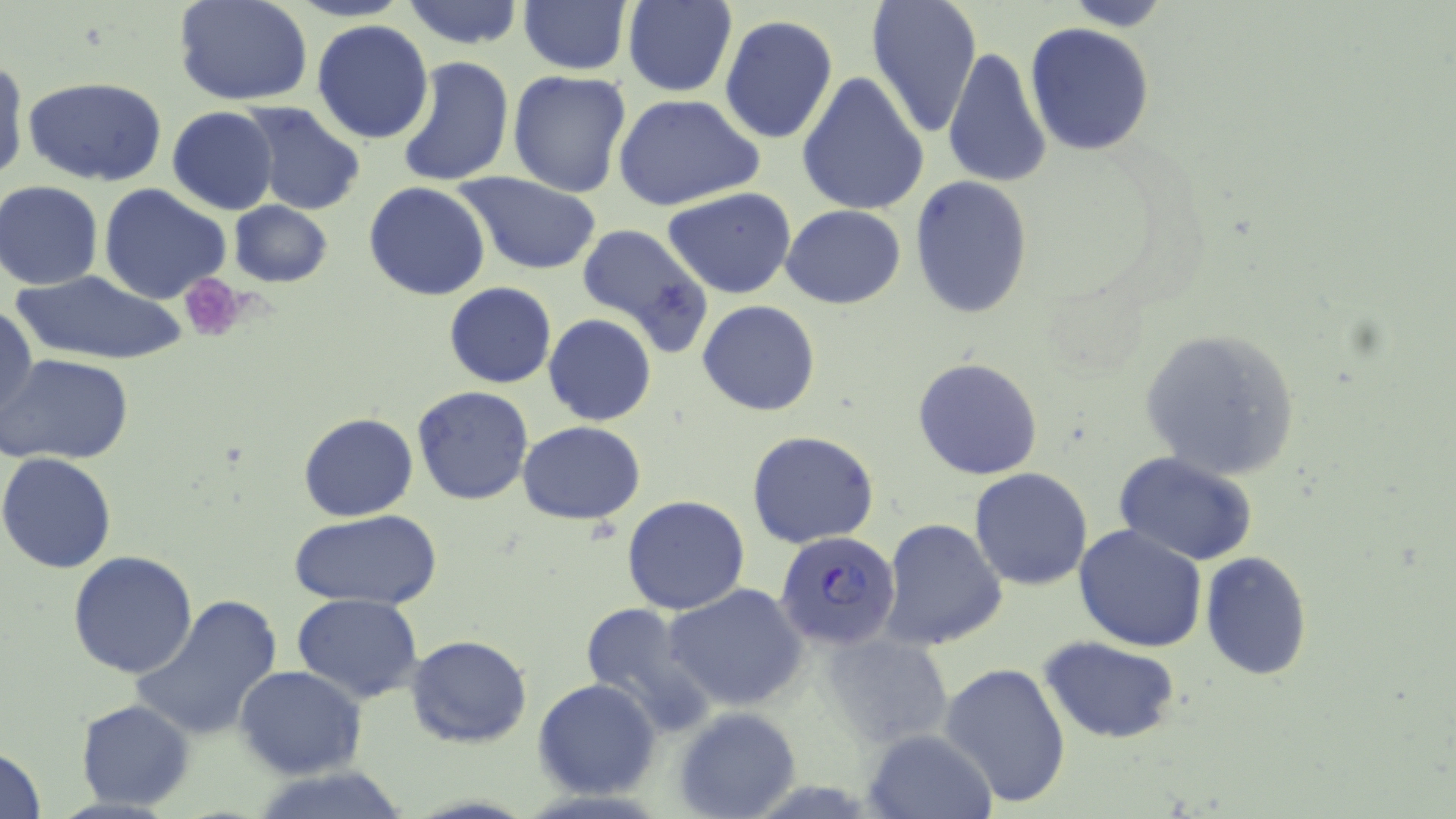
slide-level diagnosis = Plasmodium falciparum
image size = 1456×819 pixels
preparation = thin blood smear
modality = light microscopy
magnification = 1000x
uninfected red blood cell locations = approximate bounding boxes as named x1/y1/x2/y2 corners in pixels: (x1=173, y1=0, x2=314, y2=105), (x1=287, y1=0, x2=413, y2=22), (x1=401, y1=0, x2=525, y2=51), (x1=865, y1=0, x2=984, y2=138), (x1=1056, y1=0, x2=1177, y2=29), (x1=622, y1=2, x2=736, y2=97), (x1=519, y1=3, x2=631, y2=75), (x1=719, y1=16, x2=839, y2=144), (x1=312, y1=19, x2=435, y2=144), (x1=1025, y1=23, x2=1155, y2=157), (x1=942, y1=46, x2=1051, y2=189), (x1=0, y1=56, x2=26, y2=186), (x1=397, y1=56, x2=514, y2=188), (x1=507, y1=71, x2=632, y2=197), (x1=797, y1=71, x2=931, y2=216), (x1=24, y1=77, x2=168, y2=186), (x1=613, y1=92, x2=764, y2=212), (x1=239, y1=101, x2=366, y2=215), (x1=167, y1=106, x2=278, y2=215), (x1=456, y1=171, x2=605, y2=274), (x1=910, y1=177, x2=1034, y2=319), (x1=1, y1=181, x2=104, y2=289), (x1=364, y1=182, x2=490, y2=301), (x1=99, y1=183, x2=231, y2=304), (x1=662, y1=187, x2=797, y2=299), (x1=229, y1=201, x2=333, y2=289), (x1=781, y1=203, x2=907, y2=308), (x1=574, y1=221, x2=714, y2=358), (x1=9, y1=271, x2=187, y2=367), (x1=444, y1=282, x2=556, y2=388), (x1=432, y1=285, x2=543, y2=493), (x1=698, y1=300, x2=821, y2=417), (x1=1, y1=304, x2=37, y2=428), (x1=542, y1=314, x2=656, y2=426), (x1=1138, y1=327, x2=1301, y2=481), (x1=1, y1=354, x2=133, y2=465), (x1=912, y1=357, x2=1044, y2=481), (x1=411, y1=385, x2=535, y2=505), (x1=299, y1=413, x2=418, y2=522), (x1=517, y1=421, x2=645, y2=524), (x1=747, y1=430, x2=879, y2=549), (x1=0, y1=452, x2=119, y2=573), (x1=1115, y1=453, x2=1258, y2=567), (x1=968, y1=468, x2=1092, y2=590), (x1=1092, y1=477, x2=1253, y2=632), (x1=621, y1=495, x2=750, y2=615), (x1=291, y1=508, x2=443, y2=609), (x1=879, y1=519, x2=1006, y2=652), (x1=1074, y1=523, x2=1207, y2=652), (x1=67, y1=551, x2=198, y2=678), (x1=1201, y1=552, x2=1313, y2=679), (x1=663, y1=583, x2=809, y2=713), (x1=291, y1=594, x2=423, y2=705), (x1=130, y1=595, x2=286, y2=742), (x1=576, y1=602, x2=714, y2=735), (x1=824, y1=627, x2=953, y2=748), (x1=406, y1=636, x2=531, y2=748), (x1=1041, y1=637, x2=1181, y2=744), (x1=940, y1=660, x2=1072, y2=809), (x1=235, y1=666, x2=366, y2=779), (x1=534, y1=678, x2=661, y2=799), (x1=75, y1=699, x2=194, y2=809), (x1=674, y1=705, x2=801, y2=819), (x1=864, y1=729, x2=994, y2=818), (x1=0, y1=746, x2=47, y2=819), (x1=248, y1=766, x2=418, y2=819)
Plasmodium falciparum-infected red blood cell locations = approximate bounding boxes as named x1/y1/x2/y2 corners in pixels: (x1=775, y1=528, x2=901, y2=649)
platelet locations = approximate bounding boxes as named x1/y1/x2/y2 corners in pixels: (x1=181, y1=275, x2=249, y2=342)
stain = May-Grünwald-Giemsa
field of view = one of a larger specimen